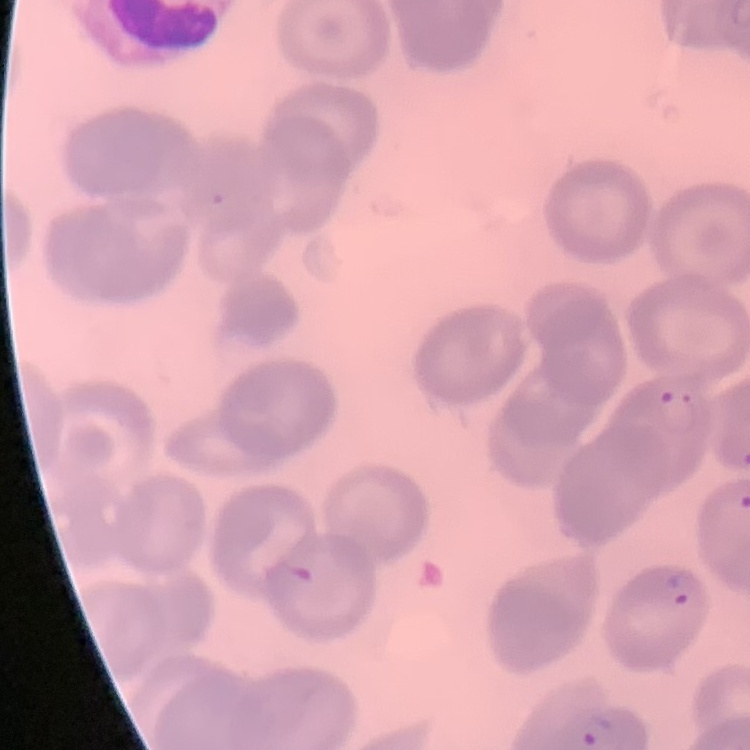
Summary:
  - Red blood cell morphology: no rouleaux formation
  - Preparation: thin peripheral smear
  - Image type: square crop of a larger photomicrograph
  - Stain: Field's or Giemsa